State the blood parasite species.
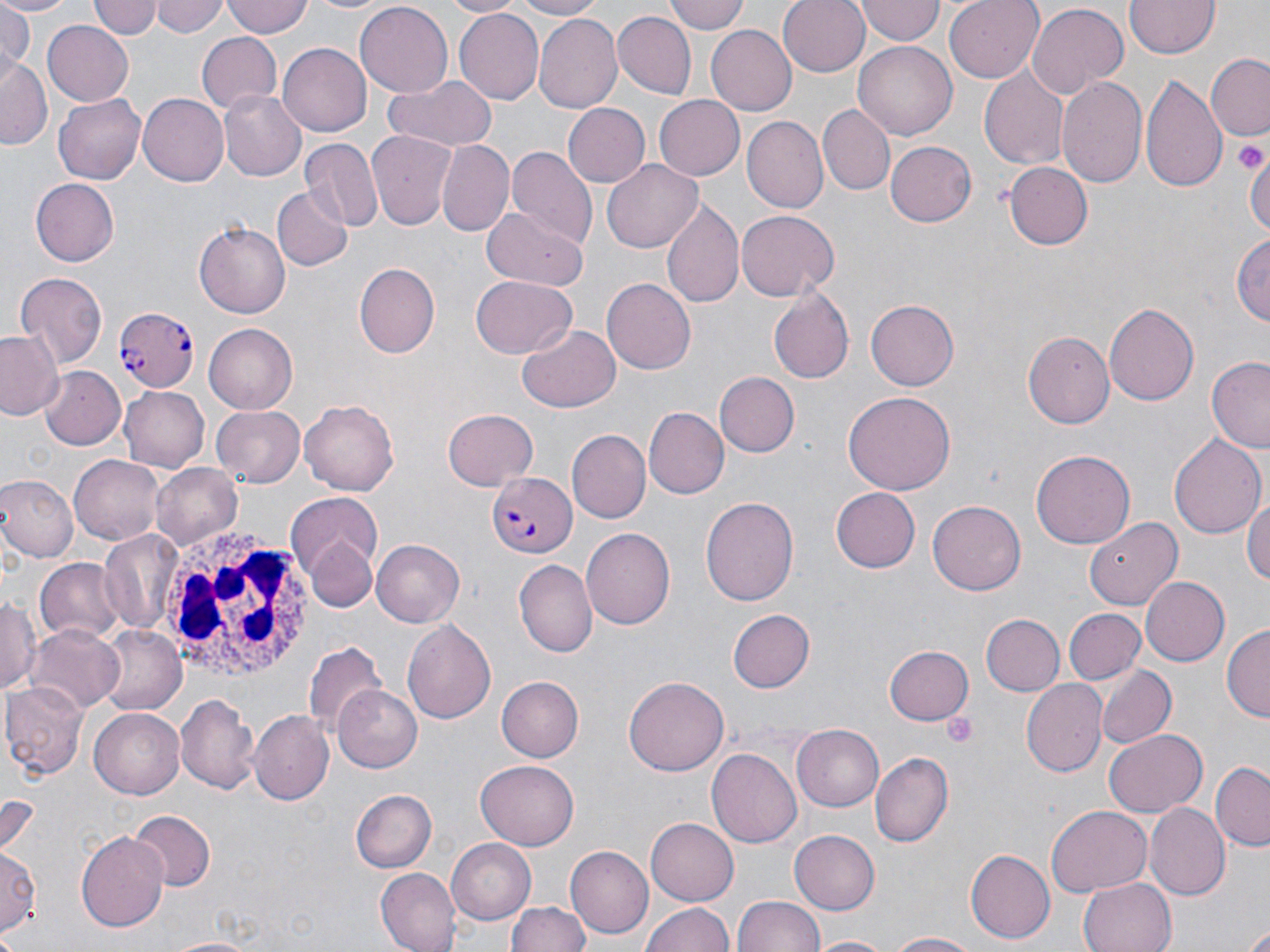

Plasmodium falciparum.

Summary:
  - Coordinate format: approximate bounding boxes as (x1, y1, x2, y2) in pixels
  - Uninfected red blood cell locations: (0, 0, 78, 17), (93, 0, 160, 41), (152, 0, 226, 38), (220, 0, 316, 42), (302, 0, 391, 15), (442, 0, 523, 17), (500, 0, 607, 19), (665, 0, 752, 36), (777, 0, 870, 76), (945, 0, 1042, 83), (1125, 0, 1222, 61), (1, 1, 35, 77), (356, 2, 452, 95), (854, 2, 944, 44), (1023, 3, 1127, 100), (453, 8, 543, 106), (533, 12, 622, 113), (613, 12, 695, 100), (41, 17, 133, 104), (706, 25, 797, 116), (197, 32, 283, 113), (853, 40, 957, 141), (277, 43, 371, 137), (1207, 56, 1268, 139), (1, 58, 51, 149), (979, 70, 1067, 170), (383, 73, 497, 152), (1143, 73, 1228, 196), (1056, 75, 1149, 191), (217, 90, 306, 182), (54, 92, 147, 184), (136, 92, 229, 187), (655, 96, 748, 179), (563, 104, 648, 187), (819, 104, 894, 195), (741, 117, 828, 214), (366, 131, 455, 230), (437, 139, 514, 236), (300, 140, 382, 234), (884, 140, 975, 227), (505, 145, 597, 244), (1246, 148, 1270, 245), (602, 159, 703, 251), (1004, 162, 1093, 248), (30, 179, 119, 266), (273, 187, 352, 271), (663, 199, 743, 308), (479, 207, 590, 292), (737, 210, 837, 300), (195, 221, 291, 318), (1233, 231, 1270, 332), (356, 262, 441, 358), (15, 272, 108, 366), (471, 275, 579, 360), (601, 277, 695, 374), (769, 286, 853, 381), (865, 299, 958, 391), (1104, 301, 1199, 405), (203, 323, 298, 414), (517, 325, 621, 412), (1024, 329, 1115, 425), (0, 331, 65, 421), (1208, 357, 1270, 452), (40, 366, 128, 450), (714, 372, 797, 457), (119, 385, 209, 471), (843, 391, 956, 495), (300, 396, 402, 495), (212, 404, 307, 487), (646, 406, 729, 497), (442, 410, 537, 490), (567, 430, 650, 522), (1167, 431, 1266, 543), (1032, 450, 1135, 548), (71, 454, 164, 543), (150, 463, 243, 549), (0, 476, 77, 562), (1244, 484, 1270, 593), (833, 486, 920, 573), (287, 495, 384, 609), (703, 495, 798, 607), (928, 500, 1025, 595), (1083, 516, 1183, 609), (581, 527, 676, 632), (99, 531, 184, 636), (371, 539, 465, 627), (35, 559, 124, 642), (514, 560, 597, 657), (1139, 576, 1229, 665), (2, 595, 40, 695), (726, 608, 813, 693), (1063, 608, 1146, 687), (980, 613, 1065, 696), (402, 620, 497, 724), (1223, 623, 1269, 724), (27, 625, 125, 713), (97, 625, 186, 714), (306, 639, 383, 734), (883, 645, 972, 725), (1096, 665, 1176, 750), (495, 675, 583, 763), (624, 676, 726, 778), (1023, 681, 1107, 776), (3, 682, 88, 780), (332, 684, 423, 774), (174, 693, 260, 796), (89, 708, 183, 798), (248, 711, 334, 805), (792, 723, 886, 811), (1103, 730, 1205, 817), (707, 748, 802, 847), (871, 753, 954, 846), (475, 761, 579, 849), (1212, 762, 1269, 849), (351, 791, 435, 873), (1046, 804, 1150, 895), (1144, 804, 1228, 900), (127, 809, 215, 890), (646, 819, 738, 903), (788, 829, 879, 915), (75, 830, 170, 933), (448, 838, 537, 925), (567, 846, 654, 939), (1, 848, 41, 940), (965, 849, 1055, 943), (375, 869, 460, 951), (1077, 875, 1177, 952), (734, 895, 825, 952), (507, 899, 592, 952), (641, 903, 736, 952), (1242, 919, 1270, 952), (883, 932, 984, 951), (806, 935, 899, 952)
  - White blood cell locations: (153, 522, 315, 685)
  - Plasmodium falciparum-infected red blood cell locations: (112, 306, 198, 395), (486, 474, 577, 559)
  - Platelet locations: (1232, 133, 1268, 179), (942, 712, 980, 748)
  - Magnification: 1000x
  - Preparation: thin blood film
  - Image size: 1270×952 pixels
  - Stain: May-Grünwald-Giemsa
  - Modality: optical microscopy
  - Field of view: one of a larger specimen